Assess this cell for malaria.
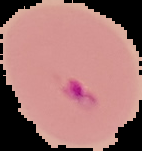

Parasitized.

From a thin blood smear. Segmented cell region on a black background. Image is 142×151 pixels.